Locate every malaria parasite and every leukocyte.
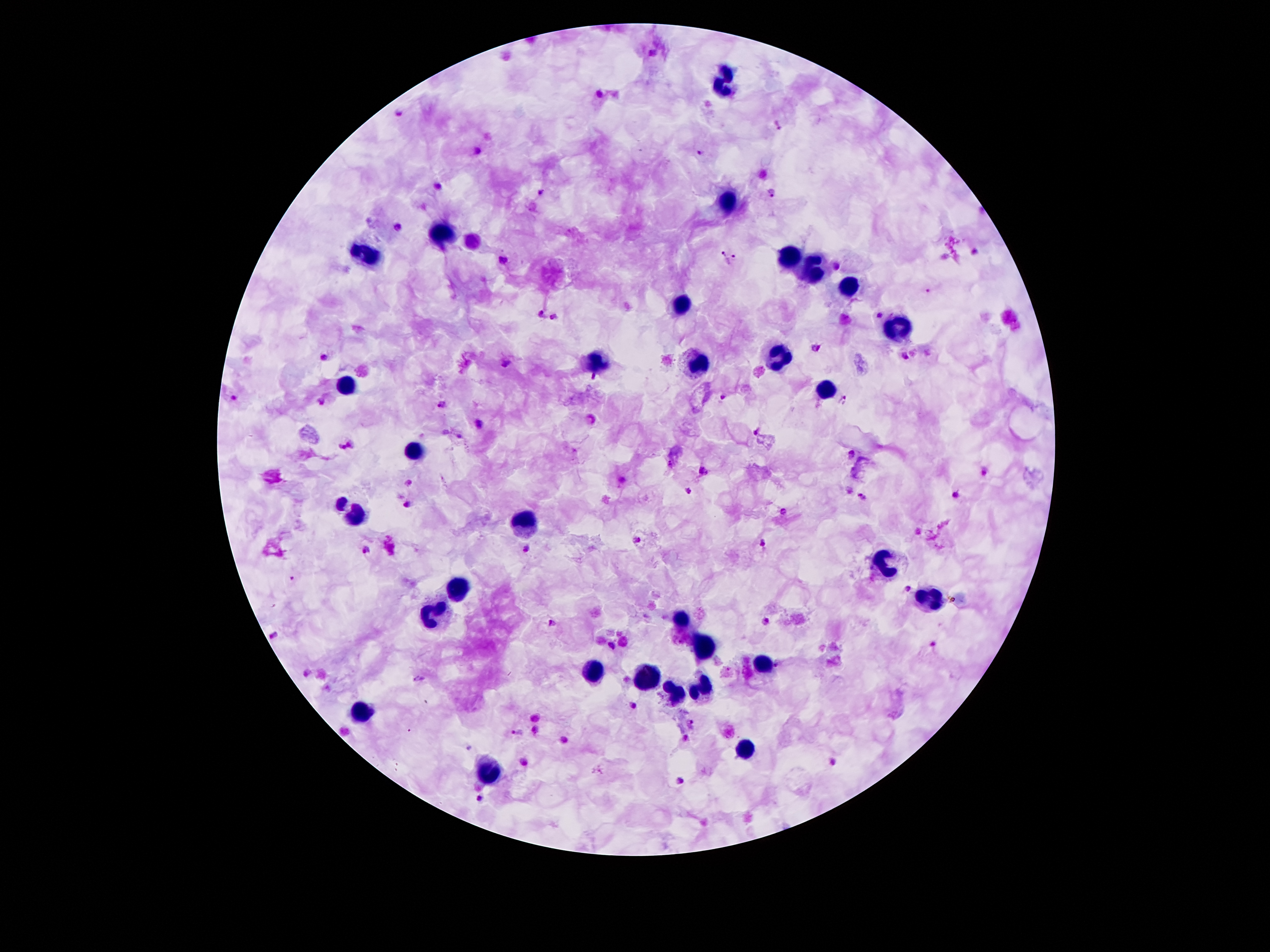
Approximate centers as [x, y] in pixels.
Malaria parasites: [652, 53], [597, 93], [401, 113], [777, 126], [478, 151], [701, 153], [439, 185], [541, 191], [770, 194], [398, 228], [972, 253], [722, 254], [731, 259], [503, 260], [837, 264], [927, 289], [542, 314], [554, 315], [880, 315], [816, 349], [323, 357], [904, 357], [506, 365], [594, 377], [235, 396], [723, 397], [842, 399], [322, 401], [441, 404], [480, 424], [756, 432], [459, 435], [352, 443], [340, 447], [852, 453], [703, 472], [984, 472], [623, 481], [409, 483], [688, 490], [957, 494], [861, 496], [408, 504], [783, 513], [638, 540], [761, 543], [526, 548], [365, 551], [292, 578], [908, 589], [765, 622], [553, 624], [276, 635], [933, 643], [612, 646], [777, 662], [307, 673], [419, 678], [633, 706], [691, 722], [519, 732], [686, 738], [469, 746], [833, 762], [681, 780], [480, 798].
Leukocytes: [720, 80], [724, 202], [441, 237], [364, 255], [788, 257], [810, 268], [846, 288], [682, 306], [894, 328], [777, 352], [596, 361], [695, 365], [346, 381], [824, 387], [413, 454], [342, 502], [360, 518], [525, 524], [881, 560], [456, 589], [931, 600], [431, 617], [681, 622], [704, 648], [768, 668], [594, 671], [646, 676], [705, 688], [679, 692], [363, 714], [746, 750], [490, 770].

Summary:
  - Magnification: 100x
  - Image size: 1270×952 pixels
  - Field of view: one from this slide
  - Capture: smartphone through the microscope eyepiece
  - Preparation: thick peripheral-blood smear
  - Patient malaria status: positive for Plasmodium falciparum
  - Stain: Giemsa